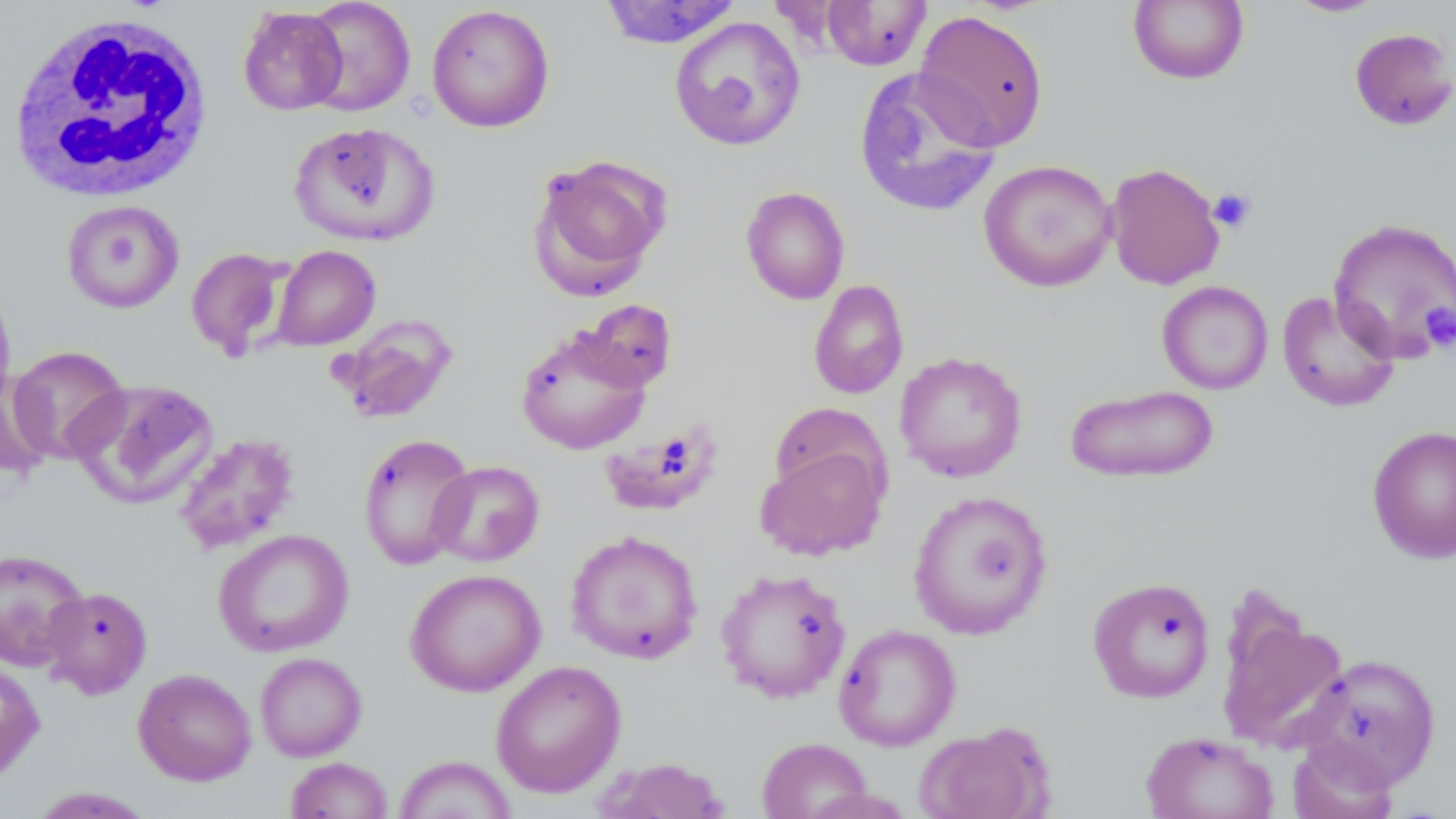
Summary:
  - Coordinate format: approximate bounding boxes as [x1, y1, x2, y2] in pixels
  - White blood cell locations: [7, 11, 214, 203]
  - Platelet locations: [1208, 188, 1256, 233], [1421, 304, 1455, 353]
  - Uninfected red blood cell locations: [302, 0, 415, 116], [599, 0, 742, 49], [1127, 0, 1250, 85], [1283, 0, 1390, 18], [820, 1, 932, 71], [426, 4, 555, 133], [237, 6, 348, 116], [912, 10, 1050, 151], [668, 16, 806, 152], [1348, 27, 1456, 132], [853, 68, 1001, 218], [288, 120, 440, 247], [527, 154, 671, 299], [978, 159, 1118, 292], [1104, 162, 1225, 290], [740, 186, 850, 305], [61, 199, 185, 313], [1326, 217, 1456, 365], [270, 245, 381, 350], [186, 247, 293, 362], [808, 279, 910, 400], [0, 281, 16, 413], [1157, 281, 1273, 395], [1277, 290, 1401, 413], [578, 299, 677, 392], [331, 314, 457, 424], [515, 326, 652, 455], [8, 345, 130, 464], [894, 351, 1028, 482], [0, 368, 55, 478], [71, 378, 220, 510], [1065, 383, 1220, 484], [597, 424, 725, 517], [1367, 425, 1456, 564], [172, 432, 300, 554], [357, 433, 475, 571], [755, 441, 888, 561], [429, 460, 545, 567], [907, 490, 1052, 639], [213, 528, 354, 657], [565, 530, 704, 665], [0, 548, 88, 671], [715, 567, 852, 703], [404, 569, 546, 697], [1087, 575, 1216, 704], [41, 586, 153, 699], [1216, 608, 1349, 752], [834, 623, 961, 750], [254, 652, 367, 761], [1298, 653, 1441, 788], [0, 658, 46, 781], [490, 660, 627, 797], [133, 668, 257, 786], [914, 721, 1054, 819], [1141, 730, 1279, 819], [756, 737, 874, 819], [1287, 738, 1401, 819], [392, 755, 517, 818], [285, 757, 393, 819], [594, 758, 732, 819], [26, 787, 158, 818]
  - Slide-level diagnosis: negative for blood parasites
  - Preparation: thin blood smear
  - Image size: 1456×819 pixels
  - Stain: May-Grünwald-Giemsa
  - Modality: light microscopy
  - Magnification: 1000x
  - Field of view: one of a larger specimen